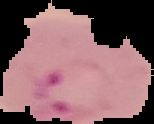

Summary:
  - Result: Plasmodium parasites identified
  - Preparation: thin blood film
  - Image type: segmented cell region with the area outside set to black
  - Image size: 154×124 pixels